State the preparation type.
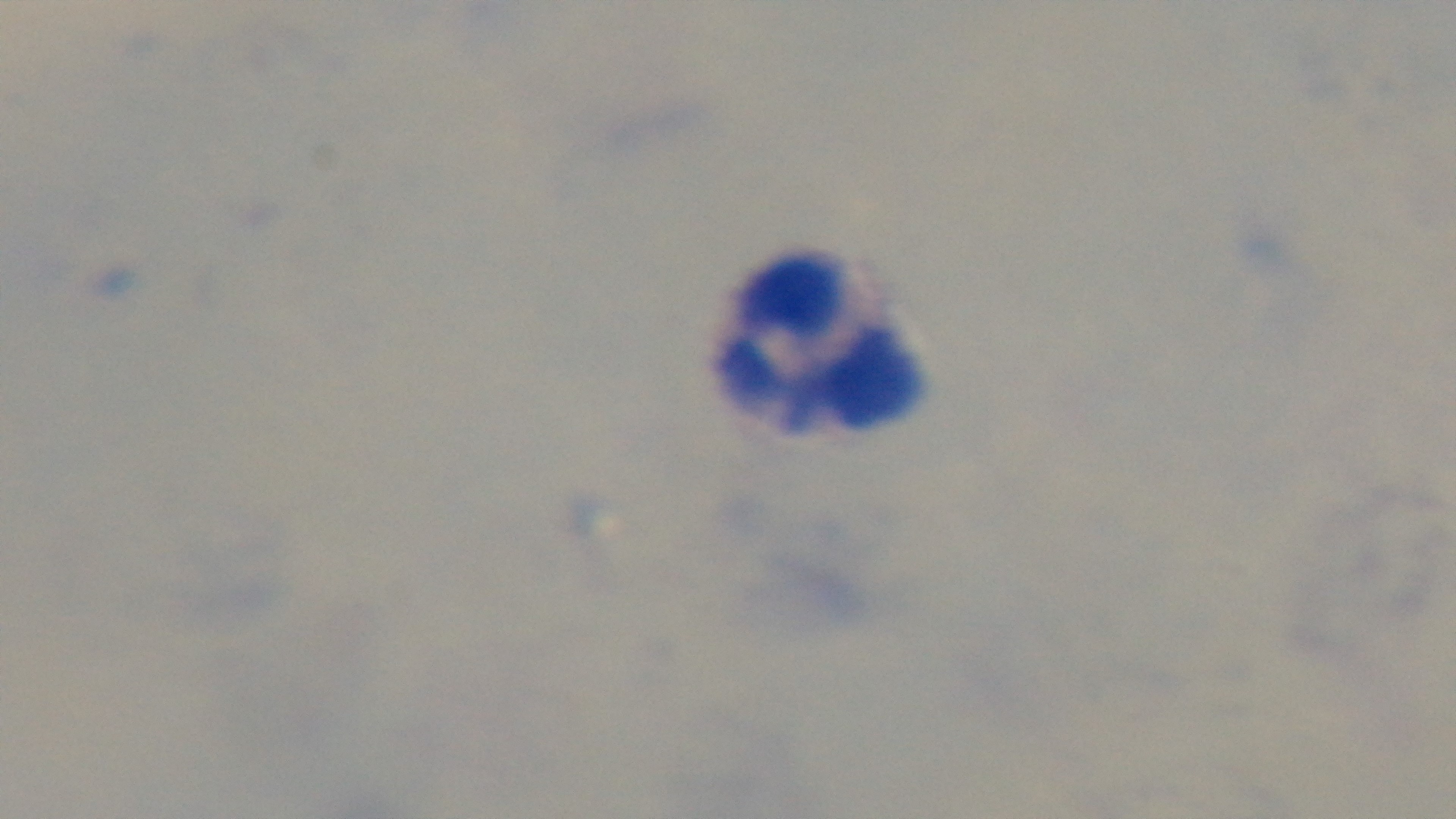

Thick.

Summary:
  - Objective: 100x oil immersion
  - Capture: mounted 4K digital camera
  - Malaria status: uninfected
  - Field of view: single
  - Modality: light microscopy
  - Stain: Giemsa